Assess the morphology of the red blood cells.
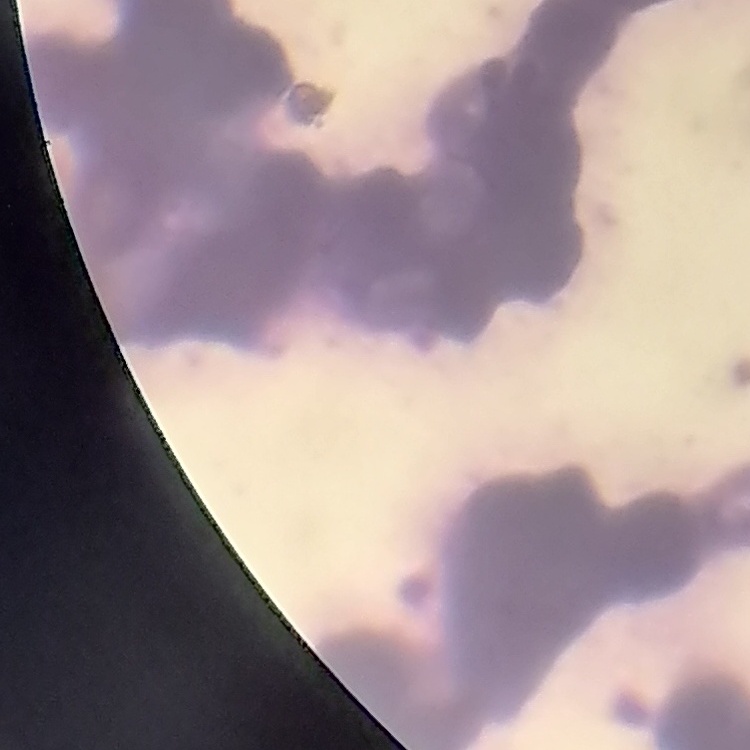
They show rouleaux formation.

preparation = thin blood smear
stain = Field's or Giemsa
image type = square crop of a larger photomicrograph